Name the parasite shown.
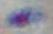

This is Toxoplasma gondii.

magnification: 1000x
modality: photomicrograph